Point out every malaria parasite and every leukocyte.
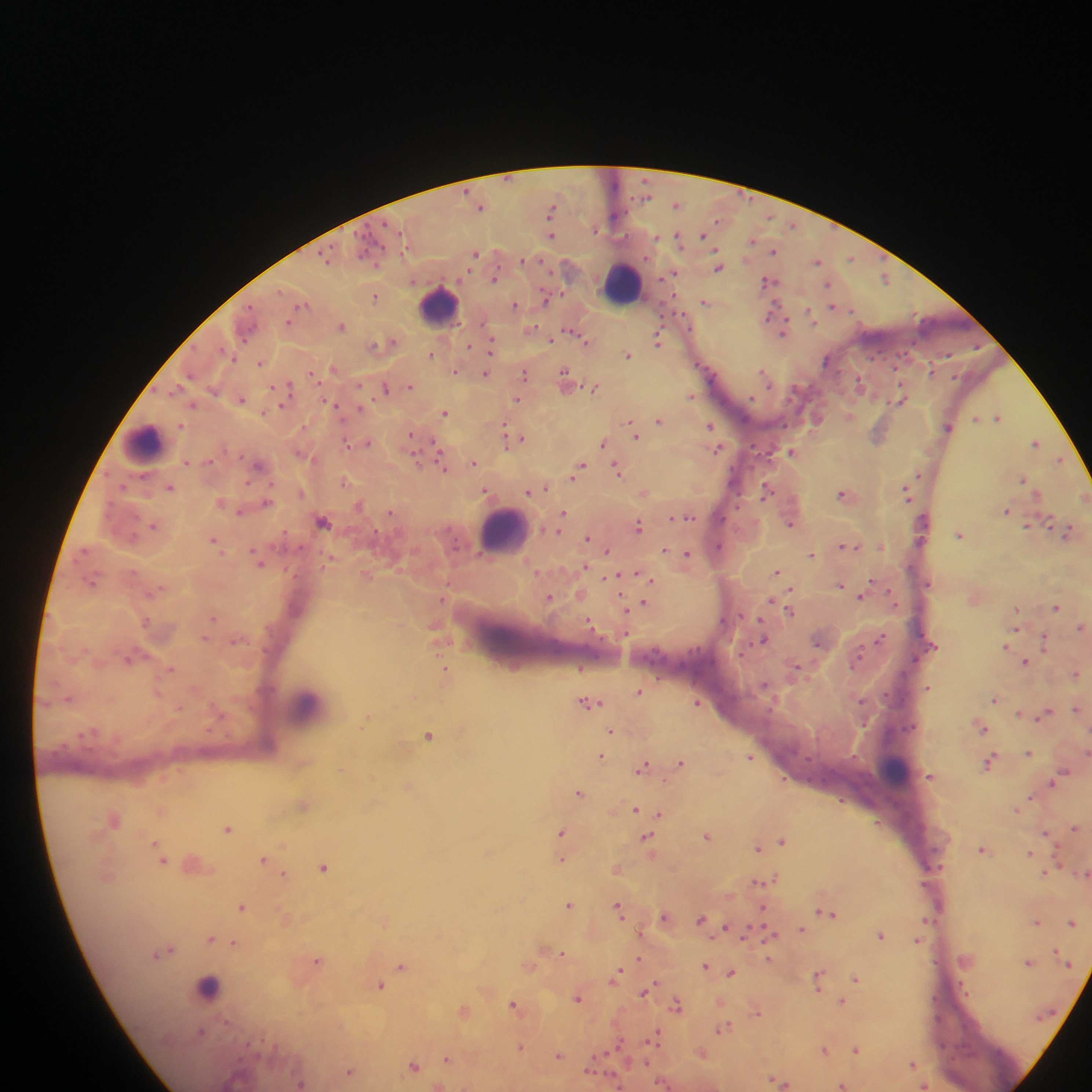
Approximate centers as {x, y} in pixels.
Malaria parasites: {647, 196}, {677, 205}, {481, 206}, {552, 208}, {615, 217}, {716, 220}, {793, 225}, {595, 230}, {552, 235}, {703, 235}, {677, 236}, {656, 238}, {751, 241}, {773, 251}, {476, 254}, {326, 257}, {851, 258}, {524, 259}, {818, 261}, {718, 268}, {673, 274}, {495, 278}, {885, 278}, {768, 281}, {828, 284}, {376, 296}, {546, 300}, {704, 302}, {304, 304}, {515, 305}, {832, 306}, {852, 309}, {772, 312}, {810, 313}, {287, 322}, {341, 326}, {532, 329}, {785, 331}, {583, 339}, {552, 340}, {658, 340}, {392, 341}, {375, 344}, {469, 346}, {491, 347}, {431, 355}, {627, 355}, {233, 357}, {827, 360}, {260, 363}, {333, 368}, {456, 371}, {708, 371}, {930, 371}, {565, 372}, {764, 372}, {485, 373}, {190, 374}, {525, 374}, {312, 375}, {566, 379}, {860, 383}, {411, 386}, {288, 387}, {385, 388}, {594, 388}, {177, 389}, {690, 396}, {241, 399}, {518, 399}, {900, 399}, {330, 403}, {192, 406}, {281, 406}, {360, 409}, {445, 413}, {850, 415}, {998, 417}, {976, 418}, {659, 420}, {818, 420}, {631, 424}, {710, 426}, {948, 427}, {879, 434}, {635, 435}, {411, 436}, {511, 436}, {519, 439}, {367, 442}, {1036, 443}, {347, 444}, {602, 444}, {436, 446}, {717, 449}, {792, 452}, {414, 460}, {1059, 460}, {186, 462}, {473, 463}, {259, 465}, {442, 466}, {581, 468}, {618, 470}, {578, 472}, {919, 475}, {1023, 480}, {343, 481}, {124, 486}, {170, 487}, {546, 488}, {485, 490}, {766, 490}, {301, 492}, {529, 492}, {644, 493}, {841, 494}, {907, 494}, {266, 502}, {360, 504}, {1006, 510}, {240, 511}, {390, 512}, {563, 513}, {688, 517}, {323, 521}, {1050, 522}, {790, 524}, {154, 525}, {1027, 525}, {639, 526}, {559, 531}, {1067, 532}, {961, 535}, {587, 538}, {214, 540}, {844, 545}, {718, 546}, {665, 550}, {607, 551}, {688, 554}, {812, 554}, {258, 559}, {586, 566}, {777, 572}, {638, 574}, {616, 577}, {647, 578}, {872, 582}, {91, 583}, {928, 584}, {840, 586}, {791, 591}, {893, 596}, {442, 598}, {550, 598}, {861, 598}, {771, 600}, {644, 604}, {1057, 607}, {626, 610}, {1016, 610}, {791, 612}, {213, 618}, {592, 625}, {1081, 627}, {1015, 629}, {880, 638}, {763, 639}, {1044, 641}, {817, 643}, {1006, 646}, {129, 659}, {857, 660}, {1026, 661}, {797, 668}, {170, 669}, {444, 671}, {1077, 674}, {765, 685}, {928, 687}, {639, 691}, {68, 698}, {995, 699}, {862, 701}, {590, 702}, {697, 703}, {179, 708}, {1076, 709}, {1019, 714}, {1046, 714}, {983, 729}, {612, 731}, {428, 735}, {1087, 752}, {1029, 753}, {601, 756}, {750, 757}, {990, 761}, {681, 762}, {643, 766}, {1064, 773}, {930, 776}, {1059, 776}, {1052, 783}, {579, 792}, {635, 810}, {661, 814}, {114, 820}, {1075, 828}, {228, 829}, {561, 832}, {1045, 833}, {707, 836}, {646, 838}, {783, 841}, {156, 843}, {758, 848}, {983, 849}, {1030, 853}, {264, 859}, {562, 860}, {162, 861}, {324, 868}, {1045, 873}, {1085, 873}, {283, 875}, {775, 878}, {761, 881}, {569, 905}, {242, 907}, {618, 908}, {826, 913}, {664, 918}, {702, 920}, {1036, 922}, {1072, 922}, {726, 927}, {802, 929}, {770, 934}, {880, 935}, {211, 939}, {918, 940}, {234, 943}, {169, 950}, {562, 952}, {1057, 952}, {157, 954}, {769, 958}, {639, 959}, {317, 961}, {1029, 962}, {402, 966}, {705, 966}, {731, 973}, {617, 974}, {856, 979}, {818, 980}, {380, 986}, {645, 991}, {578, 998}, {842, 1002}, {513, 1004}, {676, 1005}, {757, 1011}, {724, 1028}, {201, 1032}, {652, 1039}, {520, 1047}, {824, 1050}, {856, 1050}, {702, 1054}, {558, 1056}, {448, 1059}, {913, 1064}, {414, 1066}, {350, 1072}, {773, 1080}, {780, 1082}, {300, 1083}, {842, 1086}, {924, 1086}.
Leukocytes (some below the resolvable threshold): {621, 282}, {438, 305}, {144, 443}, {503, 531}, {305, 706}, {897, 770}, {208, 987}.

field of view = single
preparation = thick blood smear
image size = 1092×1092 pixels
capture = mobile-phone photograph through a microscope
country = Ghana